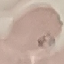
Summary:
  - Malaria status: parasitized
  - Stain: Giemsa
  - Capture: smartphone through the microscope eyepiece
  - Image type: cell patch, automatically extracted from a larger field of view and resized to 64 × 64 pixels
  - Preparation: thin smear